Comment on the morphology of the red blood cells.
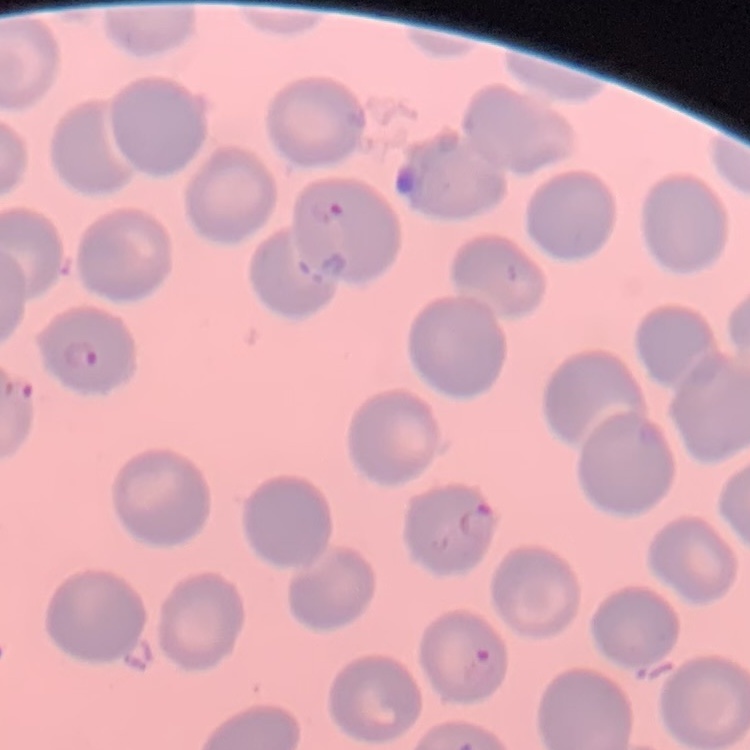

They show no rouleaux formation.

Summary:
  - Preparation: thin peripheral smear
  - Stain: Field's or Giemsa
  - Image type: square crop of a larger photomicrograph